Assess this cell for malaria.
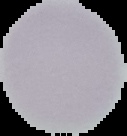

Uninfected.

From a thin blood smear. Image is 127×136 pixels. Cell region segmented out of the field of view; the surrounding area is masked to black.